State which parasite is depicted.
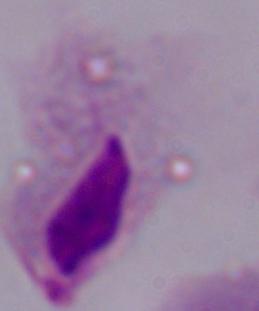
This is a trichomonad.

modality = photomicrograph
magnification = 1000x